State which parasite is depicted.
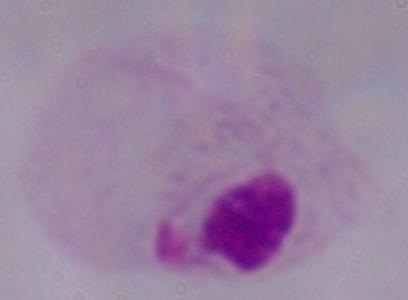

This is a trichomonad.

Micrograph. 1000x magnification.